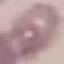
Result: no malaria parasites seen. Cell patch, automatically extracted from a larger field of view and resized to 64 × 64 pixels. Giemsa stain. Thin blood film. Photographed with a smartphone camera at the microscope eyepiece.